Describe the morphology of the red blood cells.
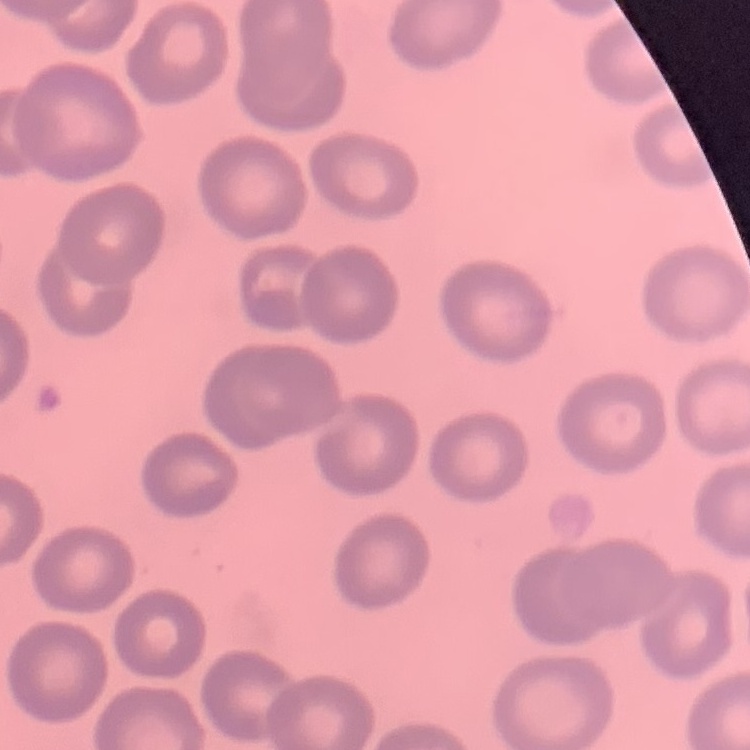
No rouleaux formation.

{
  "preparation": "thin blood film",
  "image_type": "square crop of a larger photomicrograph",
  "stain": "Field's or Giemsa"
}